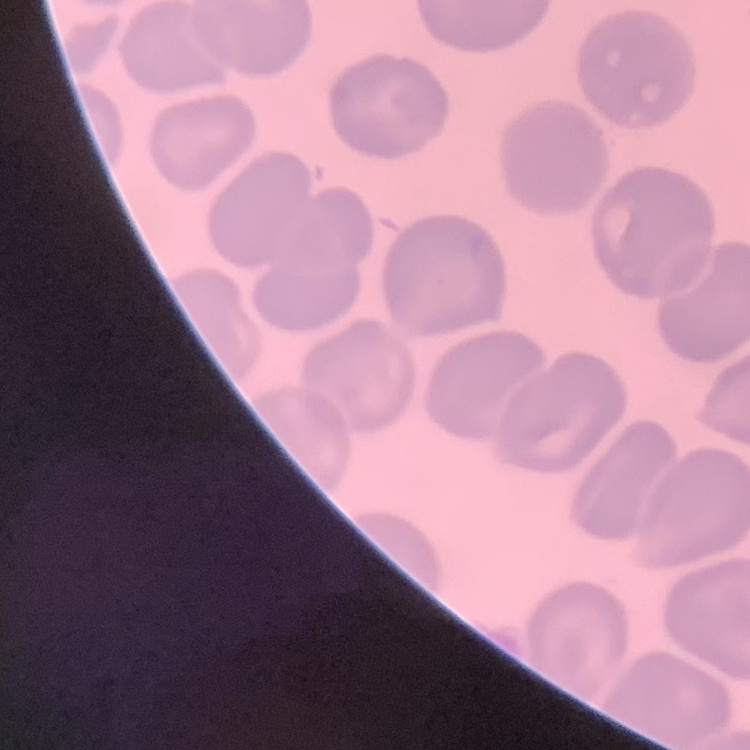
Summary:
  - Erythrocyte morphology: no rouleaux formation
  - Image type: square crop of a larger photomicrograph
  - Preparation: thin peripheral smear
  - Stain: Field's or Giemsa